Point out each leukocyte.
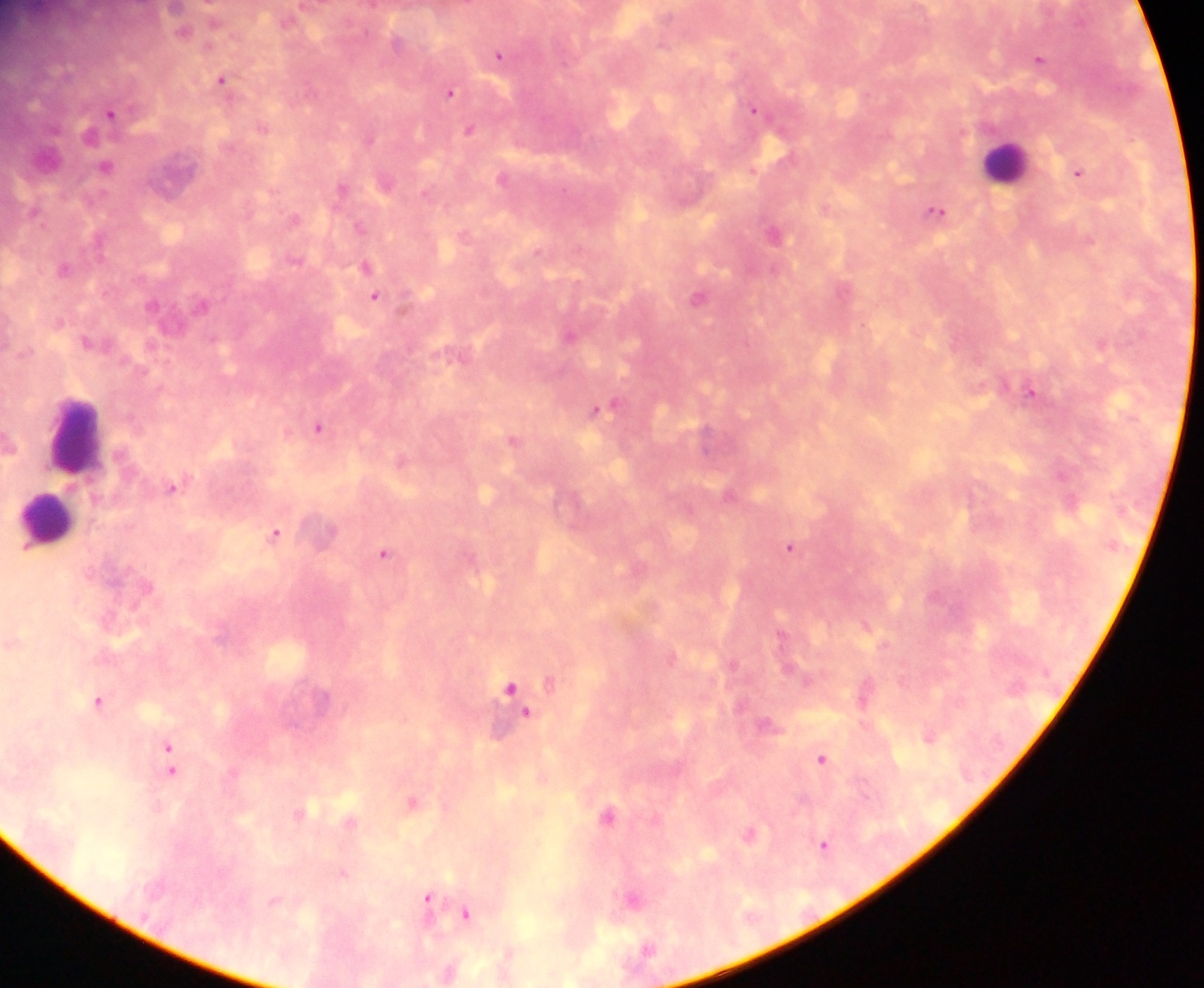

Approximate centers as x y in pixels.
Leukocytes: 1006 161; 75 433; 48 519.

Malaria parasite locations: 499 54; 1039 58; 221 78; 450 91; 754 109; 112 111; 469 128; 370 139; 106 165; 1078 173; 342 187; 936 210; 359 225; 366 268; 65 269; 375 295; 698 297; 569 334; 1102 344; 1030 391; 604 406; 318 427; 512 437; 172 486; 276 533; 790 546; 384 552; 865 624; 513 691; 864 693; 98 701; 929 735; 167 749; 822 758; 170 764; 412 801; 608 814; 749 833; 824 844; 634 899; 427 903; 466 914. Single field of view. Sample from Ghana. Photographed through a microscope with a mobile-phone camera. Image is 1204×988 pixels. Thick blood smear.